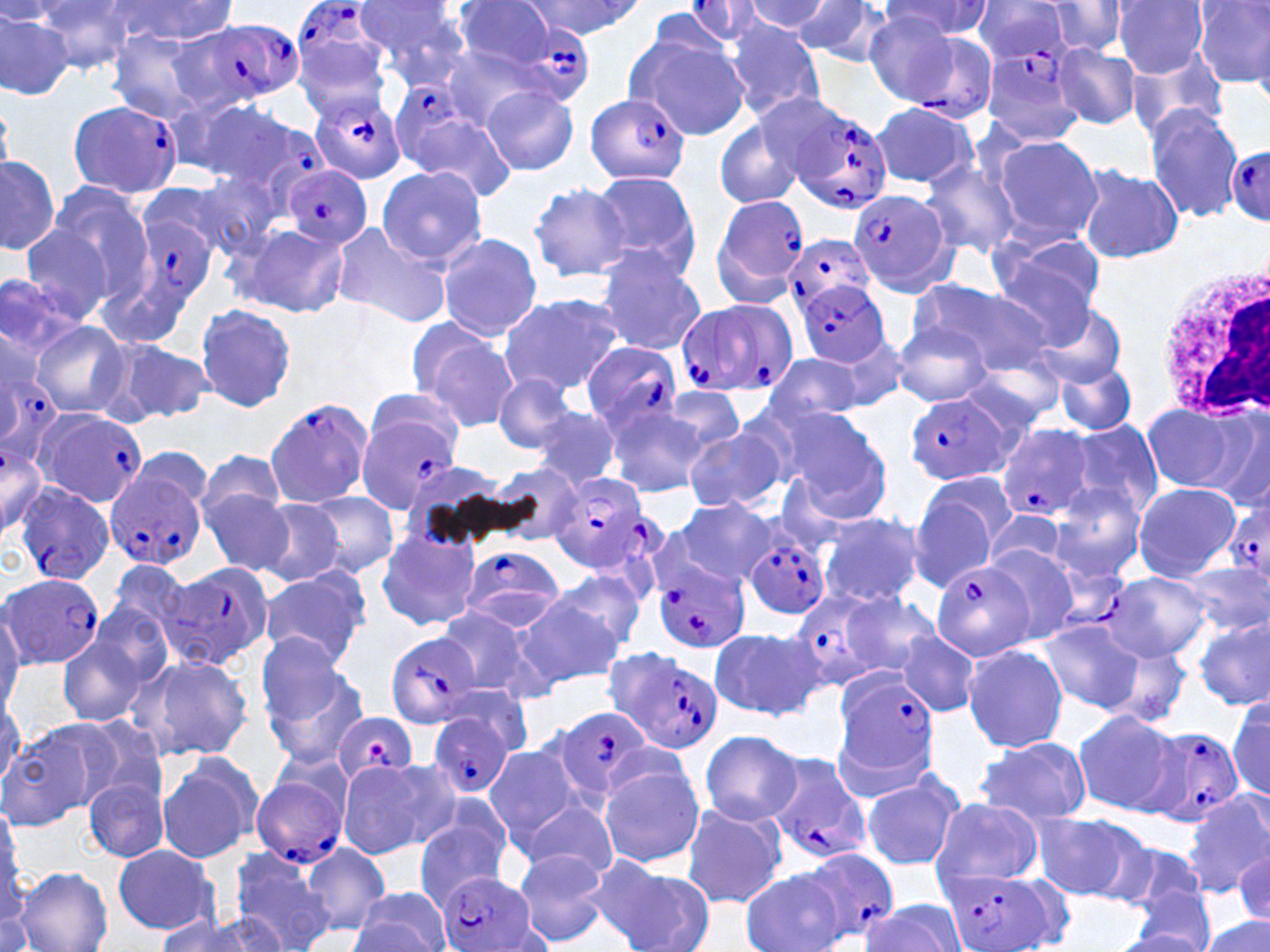
slide_level_diagnosis: Plasmodium falciparum
preparation: thin blood film
uninfected_red_blood_cell_locations: 'approximate bounding boxes as (x1,y1)-(x2,y2) corner pairs in pixels: (355,0)-(474,84), (451,0)-(561,71), (744,0)-(833,31), (972,0)-(1075,67), (1112,0)-(1207,78), (33,1)-(137,74), (109,1)-(239,46), (523,1)-(642,38), (790,1)-(895,64), (884,1)-(993,41), (1193,2)-(1270,90), (1040,3)-(1131,57), (863,10)-(963,106), (0,11)-(74,99), (721,19)-(827,119), (108,29)-(221,121), (626,30)-(747,139), (1052,44)-(1142,127), (439,46)-(554,130), (1127,49)-(1232,142), (482,85)-(578,177), (182,95)-(302,189), (868,101)-(978,190), (1144,107)-(1243,221), (394,113)-(513,196), (715,118)-(805,209), (988,134)-(1103,245), (0,154)-(59,257), (920,158)-(1022,259), (1076,162)-(1184,265), (376,164)-(487,265), (191,170)-(287,256), (588,171)-(700,278), (136,180)-(248,272), (528,182)-(632,282), (46,183)-(158,304), (329,221)-(454,328), (233,224)-(350,319), (20,226)-(115,321), (988,230)-(1109,330), (437,233)-(543,340), (594,248)-(706,356), (0,274)-(87,361), (916,280)-(1058,373), (499,291)-(623,396), (1028,301)-(1128,387), (195,303)-(297,415), (30,322)-(130,418), (892,323)-(994,408), (413,325)-(519,431), (95,338)-(208,426), (762,354)-(868,430), (960,358)-(1065,434), (1053,361)-(1138,434), (493,373)-(577,452), (657,386)-(746,463), (603,399)-(711,498), (1141,401)-(1252,493), (530,403)-(621,491), (1203,406)-(1270,513), (775,407)-(894,519), (1068,418)-(1164,519), (684,425)-(786,512), (197,451)-(288,529), (492,464)-(586,544), (908,476)-(1013,586), (1049,483)-(1147,580), (1132,483)-(1241,581), (203,490)-(293,575), (305,492)-(399,577), (668,495)-(778,586), (252,499)-(347,586), (980,511)-(1075,580), (818,512)-(924,608), (375,528)-(482,631), (981,544)-(1081,645), (105,561)-(192,646), (1181,564)-(1266,636), (548,568)-(645,656), (257,569)-(370,670), (1111,571)-(1212,662), (837,594)-(943,677), (510,595)-(622,691), (436,605)-(539,699), (0,609)-(24,713), (1195,616)-(1269,710), (1039,619)-(1145,714), (56,627)-(157,729), (708,628)-(825,721), (900,632)-(982,715), (253,633)-(346,728), (1091,634)-(1193,726), (963,643)-(1068,752), (127,653)-(254,762), (261,659)-(371,770), (0,680)-(24,783), (1228,694)-(1270,800), (1072,710)-(1183,816), (0,723)-(107,831), (699,729)-(801,826), (975,737)-(1089,822), (483,747)-(579,842), (156,753)-(262,863), (338,758)-(454,858), (598,761)-(703,869), (860,767)-(966,874), (83,774)-(170,863), (1182,791)-(1270,897), (517,798)-(618,882), (930,798)-(1043,889), (678,802)-(788,909), (0,803)-(24,914), (1031,813)-(1150,902), (411,819)-(511,909), (1118,841)-(1212,921), (300,842)-(390,936), (111,844)-(220,935), (510,847)-(610,948), (226,850)-(333,952), (1233,851)-(1268,928), (591,859)-(712,952), (13,867)-(113,951), (0,870)-(34,952), (741,872)-(842,952), (351,887)-(454,952), (1127,888)-(1215,952), (1217,892)-(1270,952), (861,898)-(969,952), (154,912)-(280,952), (1200,917)-(1268,952)'
plasmodium_falciparum_infected_red_blood_cell_locations: 'approximate bounding boxes as (x1,y1)-(x2,y2) corner pairs in pixels: (267,0)-(397,109), (683,1)-(771,47), (176,19)-(303,110), (506,23)-(591,103), (899,25)-(998,119), (977,45)-(1085,148), (391,84)-(477,165), (308,89)-(407,185), (587,92)-(691,184), (66,99)-(181,200), (784,102)-(893,214), (1227,145)-(1270,222), (281,167)-(371,249), (847,189)-(955,295), (710,193)-(810,304), (120,199)-(225,319), (783,232)-(875,315), (796,280)-(889,368), (684,299)-(797,395), (0,335)-(62,446), (581,341)-(683,434), (906,393)-(1019,486), (264,397)-(374,508), (355,406)-(463,512), (31,407)-(147,510), (995,423)-(1095,522), (104,465)-(208,571), (548,471)-(659,573), (14,482)-(114,586), (1226,491)-(1270,594), (744,534)-(831,619), (461,547)-(565,629), (1048,559)-(1129,629), (653,562)-(752,653), (161,563)-(272,666), (930,563)-(1032,660), (0,572)-(107,669), (783,587)-(904,692), (385,630)-(483,728), (614,652)-(725,757), (831,668)-(940,780), (551,705)-(658,804), (330,711)-(420,784), (427,712)-(516,799), (1143,727)-(1245,827), (767,754)-(874,867), (249,765)-(350,870), (800,847)-(898,946), (941,866)-(1060,952), (442,872)-(539,952)'
stain: May-Grünwald-Giemsa
field_of_view: one of a larger specimen
magnification: 1000x
modality: light microscopy
white_blood_cell_locations: 'approximate bounding boxes as (x1,y1)-(x2,y2) corner pairs in pixels: (1152,260)-(1270,424)'
image_size: 1270×952 pixels